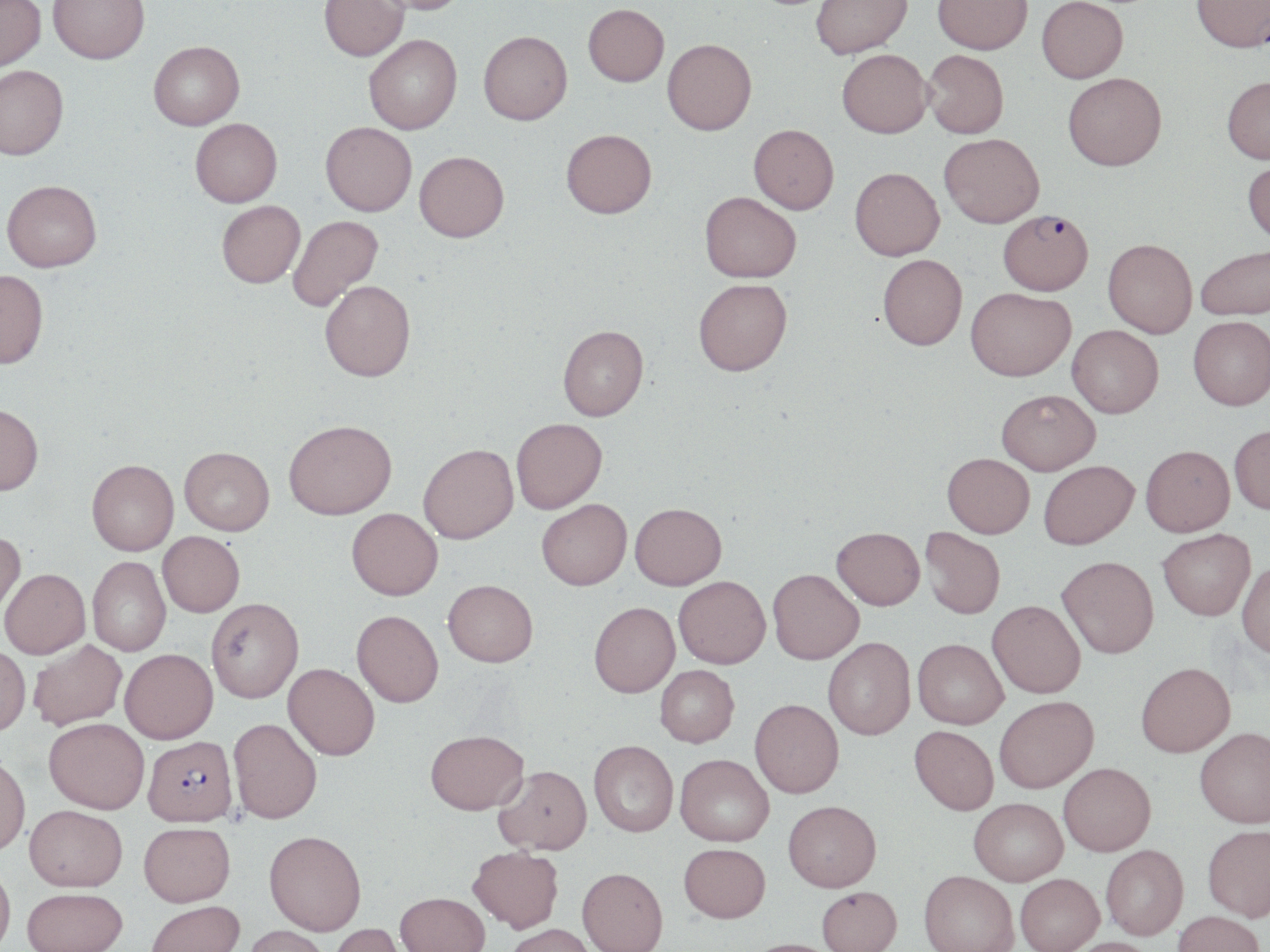
slide_level_diagnosis: Plasmodium falciparum
uninfected_red_blood_cell_locations: 'approximate bounding boxes as named x1/y1/x2/y2 corners in pixels: (x1=0, y1=0, x2=46, y2=75), (x1=48, y1=0, x2=150, y2=67), (x1=319, y1=0, x2=409, y2=64), (x1=370, y1=0, x2=471, y2=18), (x1=812, y1=0, x2=914, y2=62), (x1=933, y1=0, x2=1032, y2=58), (x1=1192, y1=0, x2=1270, y2=57), (x1=1037, y1=1, x2=1128, y2=87), (x1=583, y1=7, x2=669, y2=90), (x1=479, y1=35, x2=573, y2=130), (x1=364, y1=38, x2=462, y2=137), (x1=662, y1=42, x2=757, y2=139), (x1=149, y1=43, x2=245, y2=133), (x1=837, y1=53, x2=933, y2=143), (x1=922, y1=53, x2=1008, y2=142), (x1=0, y1=67, x2=69, y2=163), (x1=1063, y1=76, x2=1167, y2=176), (x1=1222, y1=80, x2=1270, y2=168), (x1=190, y1=122, x2=282, y2=210), (x1=320, y1=125, x2=416, y2=219), (x1=748, y1=128, x2=839, y2=218), (x1=561, y1=134, x2=657, y2=223), (x1=939, y1=137, x2=1044, y2=232), (x1=414, y1=156, x2=509, y2=246), (x1=1242, y1=162, x2=1270, y2=250), (x1=850, y1=171, x2=945, y2=264), (x1=2, y1=181, x2=103, y2=274), (x1=699, y1=196, x2=801, y2=287), (x1=217, y1=202, x2=305, y2=291), (x1=288, y1=217, x2=384, y2=312), (x1=1102, y1=243, x2=1197, y2=341), (x1=1196, y1=248, x2=1270, y2=325), (x1=878, y1=258, x2=967, y2=355), (x1=0, y1=270, x2=49, y2=368), (x1=319, y1=282, x2=416, y2=384), (x1=693, y1=283, x2=792, y2=381), (x1=965, y1=292, x2=1076, y2=386), (x1=1188, y1=320, x2=1270, y2=414), (x1=558, y1=327, x2=648, y2=422), (x1=1067, y1=328, x2=1163, y2=422), (x1=997, y1=393, x2=1100, y2=476), (x1=0, y1=404, x2=43, y2=495), (x1=511, y1=418, x2=607, y2=512), (x1=284, y1=419, x2=397, y2=518), (x1=1230, y1=426, x2=1270, y2=516), (x1=418, y1=443, x2=518, y2=543), (x1=179, y1=446, x2=274, y2=535), (x1=1140, y1=446, x2=1235, y2=539), (x1=943, y1=452, x2=1033, y2=539), (x1=87, y1=459, x2=178, y2=555), (x1=1038, y1=461, x2=1138, y2=551), (x1=536, y1=499, x2=631, y2=590), (x1=630, y1=503, x2=726, y2=590), (x1=347, y1=508, x2=442, y2=599), (x1=831, y1=526, x2=925, y2=609), (x1=920, y1=526, x2=1005, y2=619), (x1=0, y1=529, x2=26, y2=622), (x1=1159, y1=529, x2=1256, y2=621), (x1=158, y1=531, x2=244, y2=616), (x1=1057, y1=556, x2=1159, y2=659), (x1=88, y1=557, x2=171, y2=656), (x1=1237, y1=561, x2=1270, y2=660), (x1=1, y1=568, x2=90, y2=658), (x1=768, y1=568, x2=864, y2=664), (x1=674, y1=576, x2=770, y2=668), (x1=443, y1=579, x2=538, y2=667), (x1=206, y1=597, x2=303, y2=702), (x1=987, y1=600, x2=1085, y2=699), (x1=589, y1=602, x2=679, y2=697), (x1=351, y1=610, x2=443, y2=706), (x1=823, y1=637, x2=915, y2=740), (x1=912, y1=638, x2=1007, y2=729), (x1=28, y1=639, x2=127, y2=730), (x1=0, y1=645, x2=31, y2=736), (x1=120, y1=648, x2=218, y2=743), (x1=1136, y1=662, x2=1235, y2=757), (x1=283, y1=663, x2=379, y2=759), (x1=655, y1=665, x2=739, y2=747), (x1=995, y1=695, x2=1098, y2=793), (x1=749, y1=698, x2=843, y2=798), (x1=44, y1=718, x2=149, y2=813), (x1=228, y1=718, x2=322, y2=823), (x1=910, y1=726, x2=998, y2=815), (x1=1195, y1=727, x2=1270, y2=828), (x1=425, y1=729, x2=527, y2=813), (x1=588, y1=740, x2=678, y2=837), (x1=675, y1=753, x2=774, y2=846), (x1=0, y1=754, x2=30, y2=856), (x1=1058, y1=762, x2=1156, y2=856), (x1=494, y1=765, x2=592, y2=854), (x1=969, y1=798, x2=1068, y2=885), (x1=783, y1=800, x2=881, y2=891), (x1=24, y1=804, x2=128, y2=891), (x1=139, y1=821, x2=235, y2=906), (x1=1202, y1=824, x2=1270, y2=921), (x1=264, y1=829, x2=366, y2=935), (x1=679, y1=843, x2=770, y2=923), (x1=1101, y1=844, x2=1189, y2=940), (x1=468, y1=846, x2=564, y2=932), (x1=0, y1=863, x2=16, y2=952), (x1=577, y1=867, x2=667, y2=952), (x1=919, y1=870, x2=1018, y2=952), (x1=1015, y1=873, x2=1104, y2=952), (x1=817, y1=886, x2=902, y2=952), (x1=22, y1=887, x2=127, y2=952), (x1=396, y1=891, x2=490, y2=952), (x1=146, y1=899, x2=245, y2=952), (x1=1173, y1=911, x2=1265, y2=952), (x1=327, y1=923, x2=410, y2=952), (x1=503, y1=923, x2=597, y2=952), (x1=240, y1=925, x2=331, y2=952), (x1=1060, y1=937, x2=1160, y2=952), (x1=738, y1=938, x2=840, y2=952)'
field_of_view: one of a larger specimen
plasmodium_falciparum_infected_red_blood_cell_locations: 'approximate bounding boxes as named x1/y1/x2/y2 corners in pixels: (x1=998, y1=214, x2=1093, y2=300), (x1=143, y1=735, x2=238, y2=826)'
modality: light microscopy
image_size: 1270×952 pixels
magnification: 1000x
stain: May-Grünwald-Giemsa
preparation: thin blood film